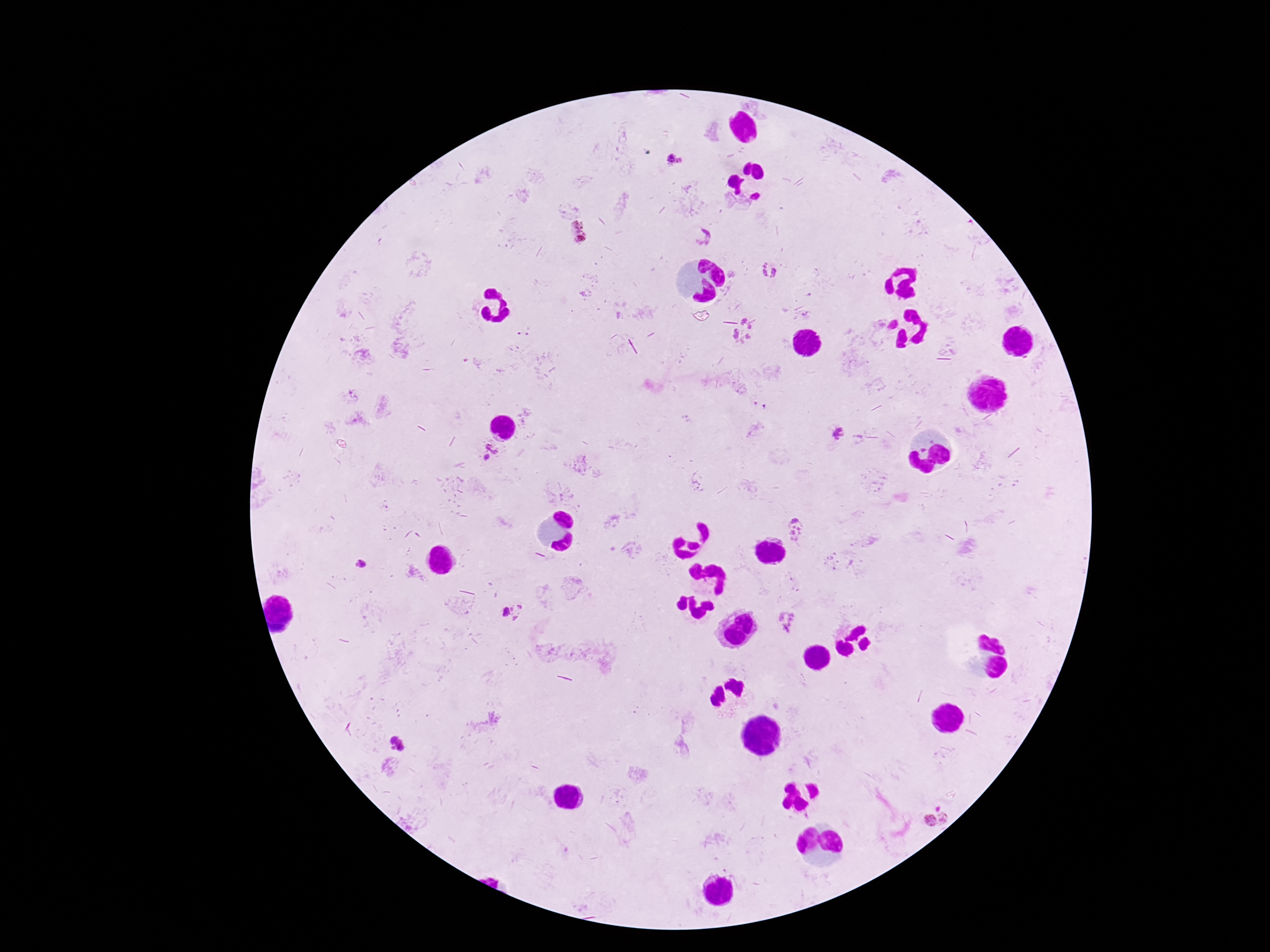

Approximate centers as {x, y} in pixels.
Summary:
  - Plasmodium parasite locations: {676, 162}, {578, 232}, {703, 237}, {769, 272}, {744, 333}, {837, 434}, {488, 452}, {796, 529}, {360, 566}, {512, 611}, {787, 621}, {397, 744}, {936, 817}
  - Capture: smartphone camera through the microscope eyepiece
  - Stain: Giemsa
  - Image size: 1270×952 pixels
  - Field of view: single
  - Preparation: thick blood smear
  - Patient malaria status: positive
  - Magnification: 100x